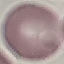 Result: no malaria parasites detected. Thin blood smear. Cell patch, automatically extracted from a larger field of view and resized to 64 × 64 pixels. Giemsa stain. Acquired by smartphone through the microscope eyepiece.